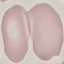

result = no malaria parasites seen
preparation = thin blood smear
capture = smartphone camera at the microscope eyepiece
stain = Giemsa
image type = automatically extracted cell patch, resized to 64 × 64 pixels